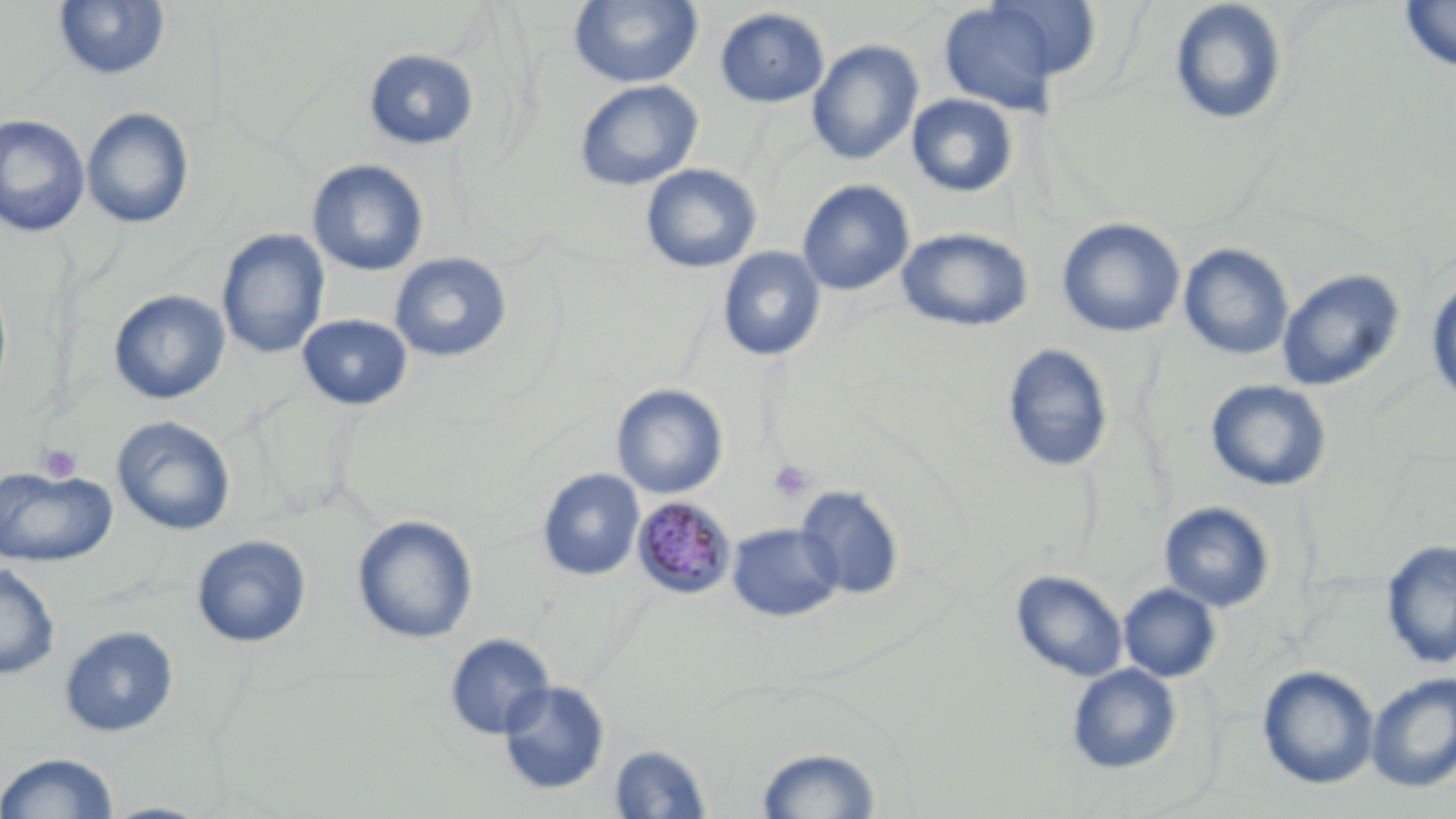
slide_level_diagnosis: Plasmodium malariae
magnification: 1000x
field_of_view: one of a larger specimen
preparation: thin blood smear
plasmodium_malariae_infected_red_blood_cell_locations: 'approximate bounding boxes as named x1/y1/x2/y2 corners in pixels: (x1=632, y1=496, x2=737, y2=599)'
image_size: 1456×819 pixels
modality: light microscopy
platelet_locations: 'approximate bounding boxes as named x1/y1/x2/y2 corners in pixels: (x1=37, y1=443, x2=83, y2=483), (x1=768, y1=459, x2=815, y2=502)'
uninfected_red_blood_cell_locations: 'approximate bounding boxes as named x1/y1/x2/y2 corners in pixels: (x1=568, y1=0, x2=704, y2=89), (x1=936, y1=0, x2=1087, y2=116), (x1=1168, y1=0, x2=1290, y2=127), (x1=53, y1=1, x2=171, y2=81), (x1=1398, y1=1, x2=1456, y2=73), (x1=714, y1=7, x2=830, y2=109), (x1=807, y1=39, x2=924, y2=166), (x1=363, y1=49, x2=480, y2=150), (x1=574, y1=79, x2=703, y2=191), (x1=907, y1=93, x2=1019, y2=198), (x1=81, y1=108, x2=196, y2=230), (x1=0, y1=114, x2=90, y2=237), (x1=306, y1=158, x2=429, y2=277), (x1=640, y1=164, x2=762, y2=273), (x1=797, y1=179, x2=915, y2=296), (x1=1057, y1=217, x2=1185, y2=338), (x1=896, y1=227, x2=1033, y2=332), (x1=217, y1=228, x2=330, y2=360), (x1=1178, y1=243, x2=1294, y2=361), (x1=717, y1=247, x2=826, y2=362), (x1=389, y1=252, x2=513, y2=362), (x1=1277, y1=268, x2=1405, y2=393), (x1=0, y1=272, x2=14, y2=409), (x1=1426, y1=274, x2=1456, y2=406), (x1=108, y1=289, x2=230, y2=405), (x1=297, y1=314, x2=413, y2=411), (x1=1001, y1=344, x2=1114, y2=472), (x1=1204, y1=379, x2=1332, y2=492), (x1=611, y1=384, x2=728, y2=499), (x1=112, y1=416, x2=237, y2=537), (x1=0, y1=465, x2=117, y2=567), (x1=537, y1=469, x2=644, y2=581), (x1=796, y1=485, x2=904, y2=600), (x1=1159, y1=501, x2=1275, y2=612), (x1=352, y1=514, x2=478, y2=645), (x1=727, y1=523, x2=843, y2=623), (x1=192, y1=534, x2=311, y2=648), (x1=1380, y1=539, x2=1456, y2=669), (x1=0, y1=561, x2=60, y2=680), (x1=1011, y1=570, x2=1128, y2=683), (x1=1118, y1=583, x2=1221, y2=683), (x1=59, y1=625, x2=179, y2=738), (x1=444, y1=633, x2=555, y2=741), (x1=1066, y1=664, x2=1182, y2=774), (x1=1257, y1=665, x2=1379, y2=790), (x1=1366, y1=672, x2=1456, y2=792), (x1=497, y1=679, x2=611, y2=796), (x1=609, y1=743, x2=713, y2=818), (x1=754, y1=744, x2=884, y2=818), (x1=1, y1=751, x2=119, y2=819), (x1=99, y1=800, x2=217, y2=818)'
stain: May-Grünwald-Giemsa